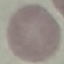
malaria status = uninfected
capture = smartphone through the microscope eyepiece
image type = cell patch, automatically extracted from a larger field of view and resized to 64 × 64 pixels
preparation = thin blood smear
stain = Giemsa